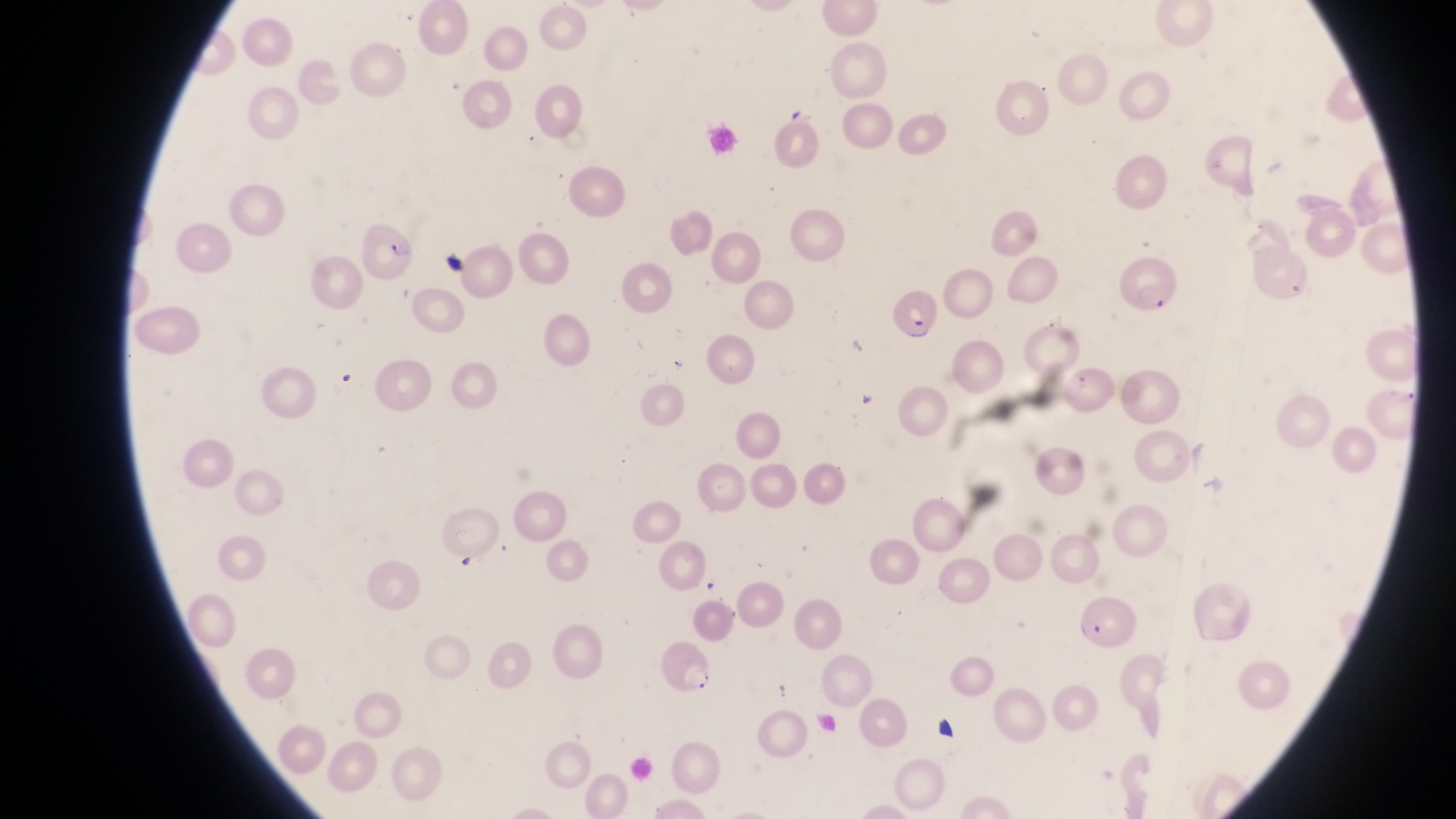 Approximate bounding boxes as left top right bottom in pixels. Artifact (platelet-like body, stain precipitate, or debris) locations: 438 244 471 276; 930 710 957 737. Parasitised red blood cell locations: 354 218 421 282; 882 281 940 341; 1072 591 1138 649; 657 639 723 695. At a magnification of 1000x. Collected in Uganda. Thin blood film. One field of view. Image is 1456×819 pixels. Photographed through the eyepiece of an Olympus CX-23 microscope with a smartphone camera.